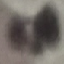 Malaria status: uninfected. Automatically extracted cell patch, resized to 64 × 64 pixels. Giemsa-stained preparation. Thin smear of blood. Photographed with a smartphone camera at the microscope eyepiece.